Locate every blood parasite and identify its species.
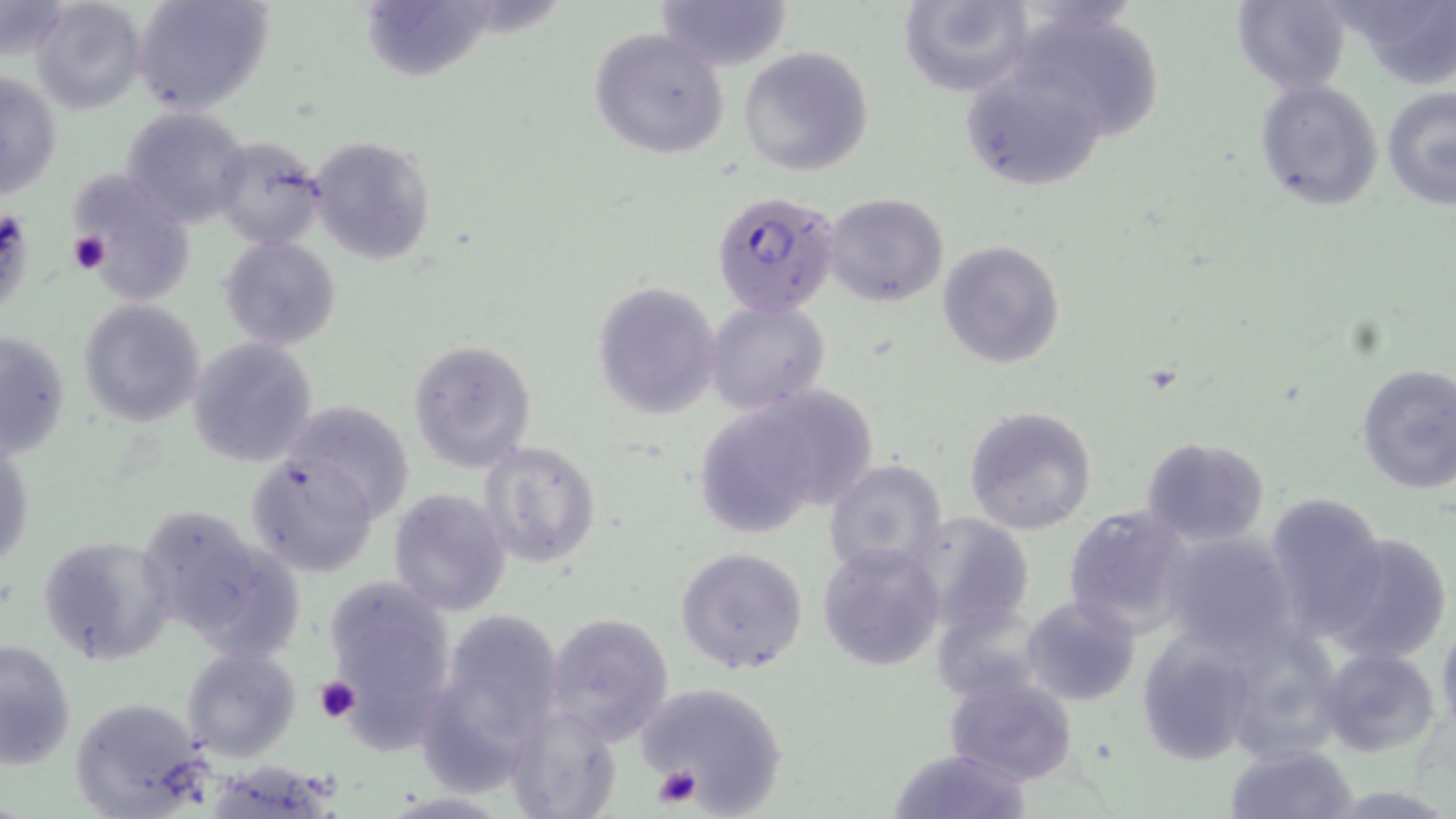
Approximate bounding boxes as (x1, y1, x2, y2) in pixels.
Plasmodium falciparum-infected red blood cells: (711, 191, 840, 319).
No Plasmodium ovale, Plasmodium malariae, Plasmodium vivax, Babesia divergens, or Trypanosoma brucei observed.

Summary:
  - Platelet locations: (68, 230, 112, 276), (313, 674, 360, 722), (651, 765, 704, 810)
  - Uninfected red blood cell locations: (28, 0, 147, 115), (131, 0, 275, 117), (652, 0, 793, 72), (898, 0, 1035, 97), (1231, 0, 1353, 93), (1334, 0, 1456, 89), (0, 3, 72, 61), (1004, 3, 1166, 142), (588, 26, 731, 159), (739, 45, 875, 176), (957, 63, 1114, 195), (1, 67, 64, 201), (1253, 77, 1384, 208), (1382, 85, 1456, 212), (120, 105, 254, 229), (209, 135, 329, 250), (308, 135, 436, 267), (71, 171, 193, 302), (822, 193, 950, 308), (218, 235, 342, 350), (937, 239, 1066, 370), (591, 281, 722, 420), (703, 298, 832, 415), (76, 299, 207, 427), (1, 329, 72, 460), (186, 337, 319, 468), (408, 338, 537, 473), (1354, 363, 1456, 493), (692, 381, 878, 532), (282, 399, 415, 523), (963, 405, 1098, 535), (1, 434, 34, 572), (1140, 436, 1272, 548), (478, 439, 601, 569), (244, 451, 381, 580), (823, 459, 948, 579), (388, 488, 511, 616), (1262, 491, 1385, 636), (133, 502, 307, 664), (1063, 504, 1197, 636), (909, 512, 1034, 636), (1158, 530, 1301, 659), (1324, 531, 1452, 664), (37, 534, 176, 665), (816, 541, 946, 671), (675, 546, 808, 677), (324, 580, 457, 740), (1021, 594, 1142, 708), (933, 603, 1048, 699), (419, 608, 568, 786), (543, 612, 674, 744), (1436, 619, 1456, 739), (1138, 634, 1260, 768), (0, 636, 78, 771), (180, 645, 303, 762), (1315, 646, 1442, 759), (942, 675, 1080, 785), (630, 680, 790, 813), (66, 694, 214, 816), (503, 704, 624, 819), (1225, 742, 1358, 819), (886, 746, 1032, 818)
  - Slide-level diagnosis: Plasmodium falciparum
  - Magnification: 1000x
  - Stain: May-Grünwald-Giemsa
  - Image size: 1456×819 pixels
  - Preparation: thin blood smear
  - Modality: light microscopy
  - Field of view: one of a larger specimen